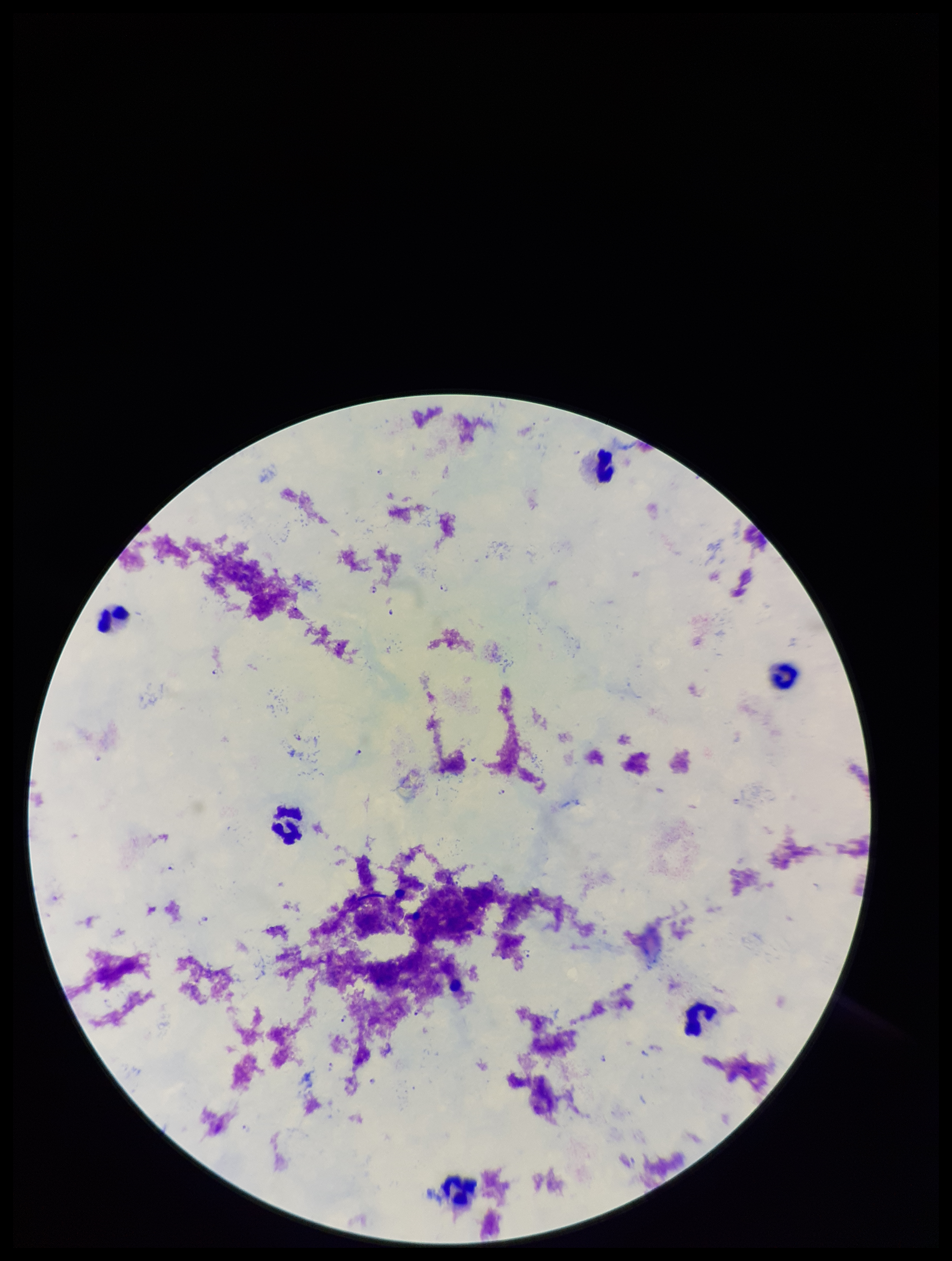

{
  "image_size": "952×1261 pixels",
  "patient_malaria_status": "infected",
  "field_of_view": "one from this slide",
  "stain": "Giemsa",
  "preparation": "thick",
  "parasite_count": 16,
  "species_reported_for_this_patient": "Plasmodium falciparum",
  "capture": "smartphone photograph through the microscope eyepiece",
  "leukocyte_count": 6,
  "plasmodium_parasites": "identified"
}